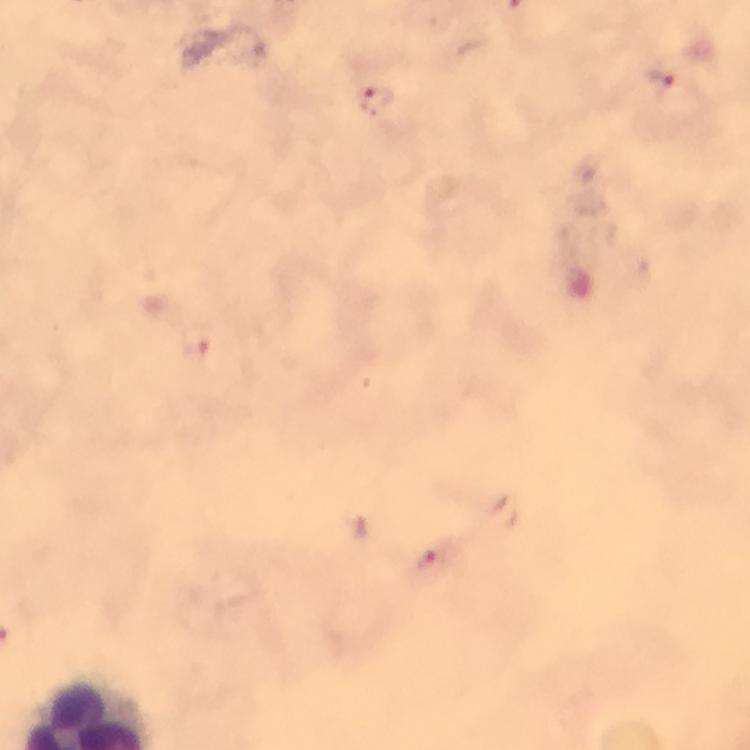
magnification: 100x
plasmodium_parasite_locations: 'approximate object centers, in pixels from the top-left corner: (x=659, y=77), (x=377, y=100), (x=432, y=561)'
cropped_from: a single field of view
preparation: thick blood film
capture: smartphone photograph through a microscope
immersion_oil: applied
image_size: 750×750 pixels
stain: Giemsa
context: from a diagnostic examination for malaria